Outline each Plasmodium falciparum-infected red blood cell.
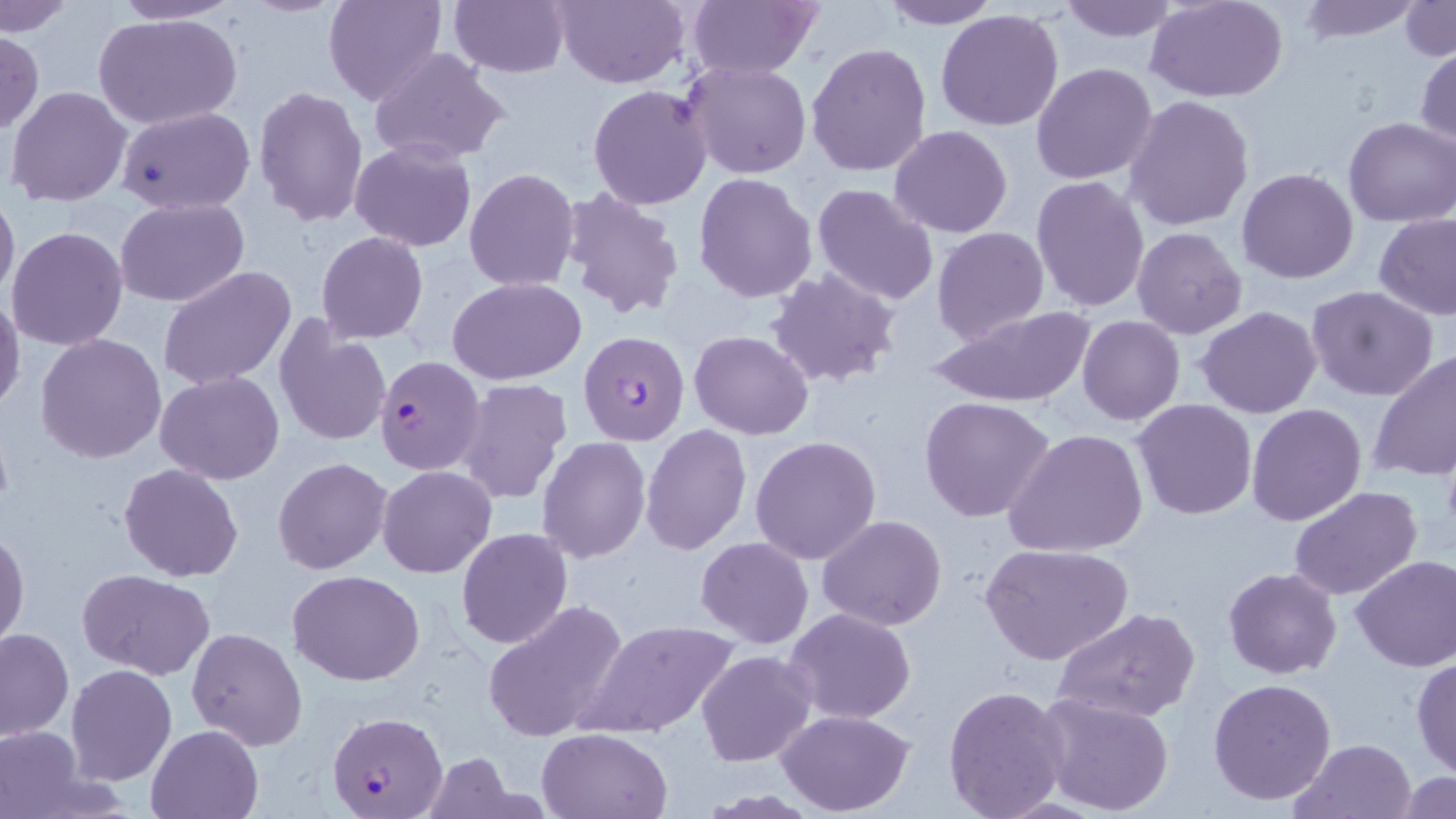
Approximate bounding boxes as named x1/y1/x2/y2 corners in pixels.
Plasmodium falciparum-infected red blood cells (subset): (x1=375, y1=356, x2=486, y2=474), (x1=329, y1=709, x2=448, y2=818).

slide-level diagnosis = Plasmodium falciparum
field of view = single
modality = light microscopy
preparation = thin blood smear
magnification = 1000x
stain = May-Grünwald-Giemsa
image size = 1456×819 pixels
uninfected red blood cell locations (subset) = approximate bounding boxes as named x1/y1/x2/y2 corners in pixels: (x1=107, y1=0, x2=244, y2=25), (x1=325, y1=0, x2=448, y2=108), (x1=447, y1=0, x2=568, y2=77), (x1=554, y1=0, x2=690, y2=89), (x1=684, y1=0, x2=822, y2=80), (x1=876, y1=0, x2=1003, y2=29), (x1=1055, y1=0, x2=1180, y2=43), (x1=1296, y1=0, x2=1424, y2=42), (x1=1148, y1=1, x2=1289, y2=102), (x1=1401, y1=1, x2=1456, y2=62), (x1=0, y1=2, x2=76, y2=35), (x1=936, y1=9, x2=1065, y2=132), (x1=96, y1=12, x2=242, y2=129), (x1=0, y1=30, x2=44, y2=137), (x1=805, y1=42, x2=931, y2=179), (x1=1414, y1=45, x2=1456, y2=154), (x1=369, y1=48, x2=510, y2=166), (x1=683, y1=60, x2=812, y2=178), (x1=1031, y1=62, x2=1159, y2=185), (x1=587, y1=84, x2=714, y2=210), (x1=6, y1=85, x2=131, y2=207), (x1=252, y1=86, x2=368, y2=227), (x1=1124, y1=96, x2=1253, y2=231), (x1=117, y1=105, x2=256, y2=214), (x1=1343, y1=116, x2=1456, y2=228), (x1=889, y1=125, x2=1013, y2=238), (x1=349, y1=140, x2=476, y2=251), (x1=463, y1=168, x2=581, y2=292), (x1=1237, y1=168, x2=1358, y2=284), (x1=693, y1=172, x2=816, y2=301), (x1=1031, y1=175, x2=1151, y2=314), (x1=811, y1=184, x2=941, y2=306), (x1=0, y1=186, x2=20, y2=305), (x1=563, y1=188, x2=687, y2=323), (x1=116, y1=197, x2=251, y2=307), (x1=1375, y1=215, x2=1456, y2=321), (x1=7, y1=226, x2=127, y2=351), (x1=1132, y1=226, x2=1248, y2=340), (x1=932, y1=227, x2=1048, y2=345), (x1=316, y1=232, x2=428, y2=343), (x1=159, y1=266, x2=298, y2=392), (x1=767, y1=268, x2=900, y2=390), (x1=448, y1=277, x2=586, y2=385), (x1=1306, y1=285, x2=1440, y2=401), (x1=0, y1=294, x2=25, y2=412), (x1=926, y1=306, x2=1097, y2=408), (x1=1197, y1=307, x2=1322, y2=419), (x1=1077, y1=315, x2=1185, y2=424), (x1=273, y1=321, x2=392, y2=449), (x1=689, y1=329, x2=814, y2=440), (x1=36, y1=333, x2=168, y2=464), (x1=1369, y1=349, x2=1456, y2=482), (x1=155, y1=371, x2=284, y2=484), (x1=456, y1=378, x2=573, y2=505), (x1=919, y1=396, x2=1055, y2=523), (x1=1132, y1=399, x2=1257, y2=520), (x1=1245, y1=404, x2=1367, y2=526), (x1=642, y1=423, x2=750, y2=555), (x1=1005, y1=427, x2=1150, y2=559), (x1=750, y1=435, x2=881, y2=564), (x1=536, y1=436, x2=651, y2=562), (x1=272, y1=457, x2=393, y2=574), (x1=118, y1=463, x2=245, y2=583), (x1=377, y1=465, x2=496, y2=578), (x1=1288, y1=485, x2=1425, y2=602), (x1=817, y1=515, x2=947, y2=630), (x1=0, y1=525, x2=28, y2=649), (x1=456, y1=528, x2=573, y2=648), (x1=694, y1=537, x2=813, y2=648), (x1=979, y1=541, x2=1133, y2=666), (x1=1349, y1=554, x2=1456, y2=672), (x1=1224, y1=567, x2=1342, y2=679), (x1=76, y1=568, x2=216, y2=677), (x1=288, y1=569, x2=425, y2=685), (x1=482, y1=599, x2=631, y2=742), (x1=1053, y1=607, x2=1199, y2=724), (x1=782, y1=608, x2=918, y2=726), (x1=576, y1=616, x2=742, y2=738), (x1=0, y1=628, x2=73, y2=741), (x1=187, y1=628, x2=307, y2=749), (x1=697, y1=651, x2=816, y2=766), (x1=1411, y1=654, x2=1456, y2=778), (x1=66, y1=664, x2=177, y2=784), (x1=1207, y1=677, x2=1337, y2=806), (x1=942, y1=686, x2=1070, y2=818), (x1=1034, y1=691, x2=1175, y2=816), (x1=775, y1=709, x2=914, y2=815), (x1=146, y1=724, x2=262, y2=818), (x1=0, y1=725, x2=90, y2=819), (x1=537, y1=728, x2=671, y2=818), (x1=1292, y1=737, x2=1418, y2=819), (x1=423, y1=754, x2=520, y2=818), (x1=1395, y1=773, x2=1456, y2=819)